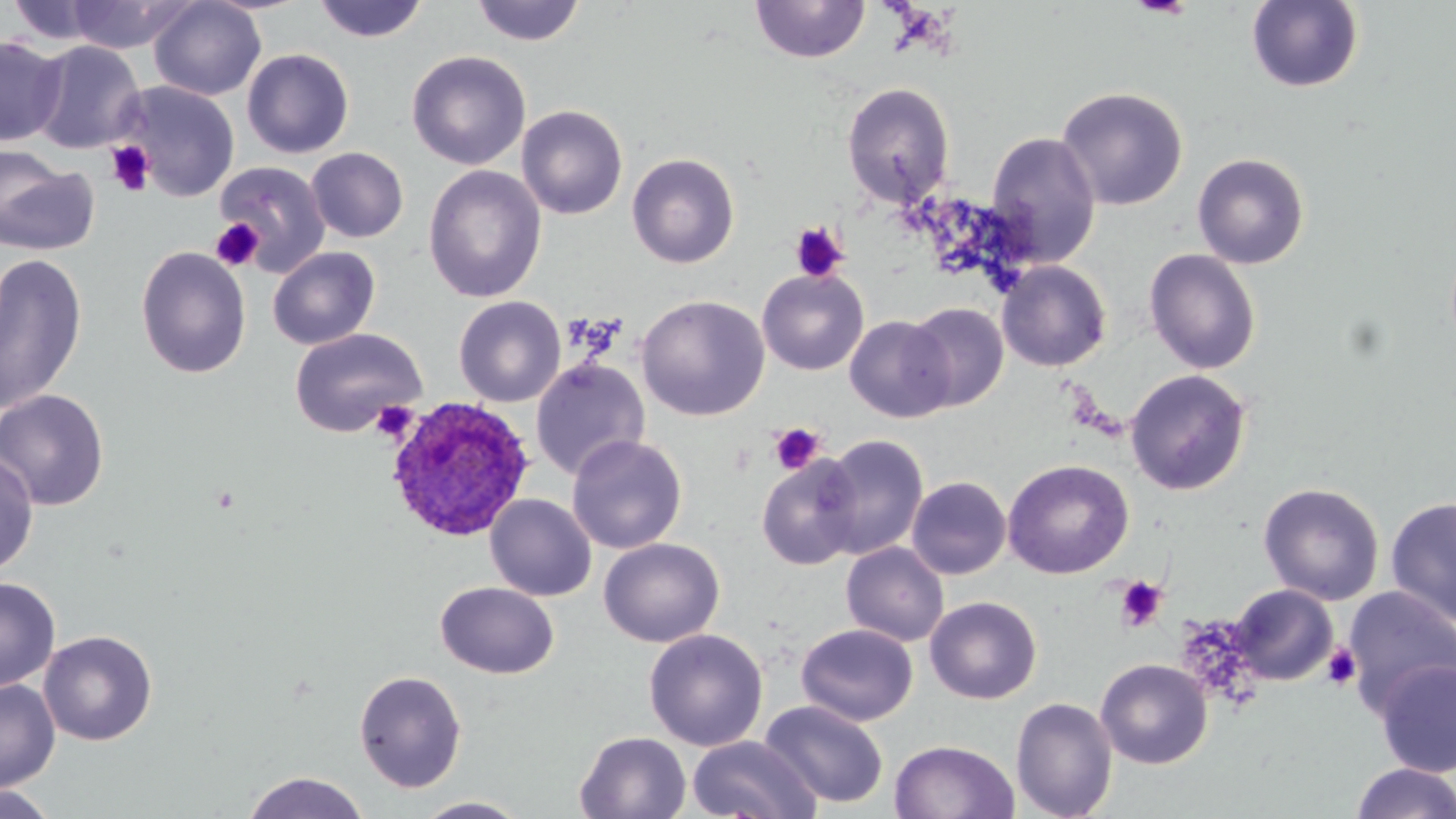
Summary:
  - Coordinate format: approximate bounding boxes as [x1, y1, x2, y2] in pixels
  - Plasmodium ovale-infected red blood cell locations: [384, 395, 535, 543]
  - Platelet locations: [106, 142, 155, 196], [212, 162, 330, 278], [210, 217, 265, 272], [789, 221, 849, 283], [370, 400, 418, 442], [768, 422, 825, 474], [1114, 575, 1167, 631], [1322, 644, 1362, 690]
  - Uninfected red blood cell locations: [62, 0, 197, 54], [312, 0, 430, 43], [750, 0, 871, 64], [4, 1, 114, 45], [148, 1, 266, 101], [470, 1, 586, 46], [1245, 1, 1365, 93], [0, 34, 66, 146], [28, 40, 146, 153], [241, 48, 354, 159], [406, 51, 531, 170], [114, 81, 240, 201], [841, 83, 955, 207], [1056, 86, 1189, 210], [516, 104, 628, 219], [985, 130, 1101, 267], [0, 147, 99, 257], [306, 147, 408, 242], [627, 152, 740, 268], [1192, 152, 1310, 269], [215, 159, 332, 276], [423, 165, 546, 302], [135, 245, 252, 379], [267, 246, 380, 350], [1144, 249, 1261, 374], [0, 252, 88, 416], [996, 260, 1112, 372], [757, 268, 868, 375], [636, 294, 770, 421], [454, 296, 566, 407], [905, 302, 1007, 412], [845, 315, 955, 422], [290, 327, 427, 437], [531, 358, 650, 481], [1125, 369, 1251, 495], [0, 388, 110, 511], [818, 434, 928, 559], [567, 435, 687, 554], [0, 449, 39, 577], [756, 454, 863, 570], [1002, 459, 1134, 579], [854, 462, 985, 592], [908, 476, 1010, 580], [1259, 482, 1384, 605], [485, 494, 596, 601], [1385, 496, 1456, 627], [599, 537, 725, 648], [841, 542, 949, 647], [1, 576, 60, 693], [435, 581, 560, 679], [1229, 584, 1338, 685], [1342, 586, 1456, 715], [925, 596, 1042, 704], [796, 623, 918, 726], [644, 628, 768, 751], [39, 630, 157, 746], [1095, 658, 1213, 769], [1374, 658, 1456, 777], [353, 669, 468, 792], [0, 679, 60, 792], [1010, 697, 1118, 818], [760, 700, 889, 808], [574, 731, 691, 818], [687, 735, 822, 818], [889, 738, 1019, 819], [1349, 762, 1456, 818], [242, 771, 370, 819], [0, 785, 60, 818], [413, 796, 530, 818]
  - Slide-level diagnosis: Plasmodium ovale
  - Magnification: 1000x
  - Field of view: single
  - Modality: light microscopy
  - Preparation: thin blood film
  - Image size: 1456×819 pixels
  - Stain: May-Grünwald-Giemsa